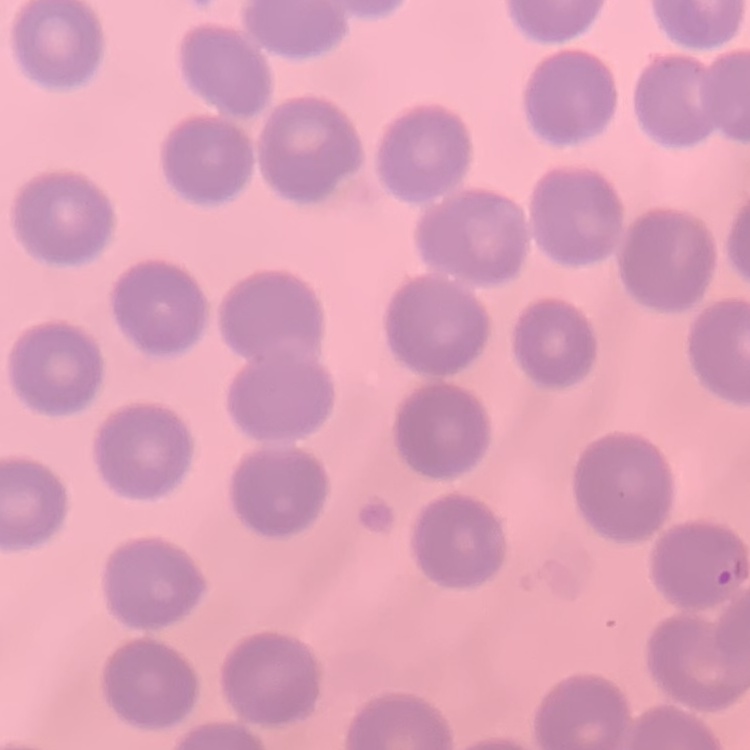 The red blood cells exhibit no rouleaux formation. Thin blood film. Field's or Giemsa stain. One tile cut from a larger photomicrograph.